Describe the morphology of the erythrocytes.
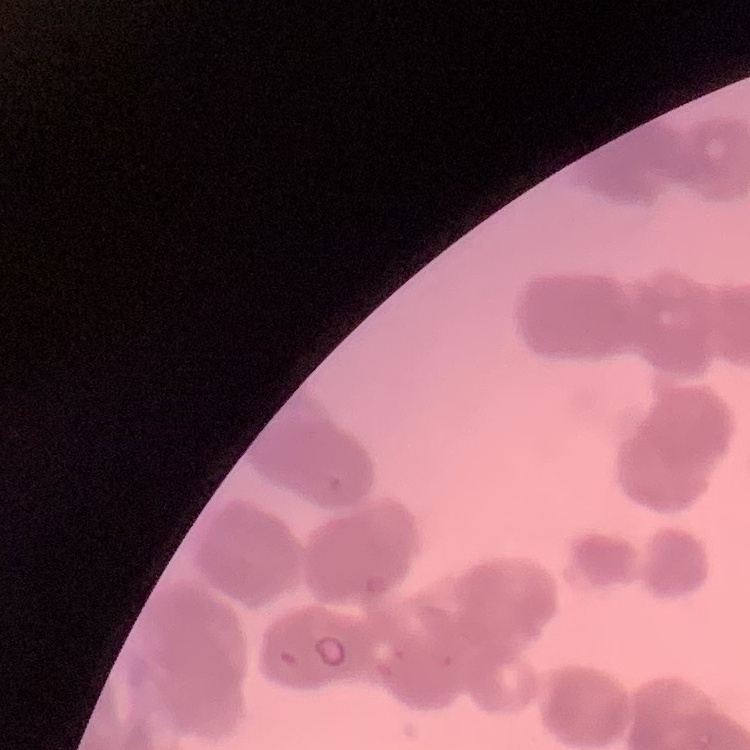

Rouleaux formation.

One tile cut from a larger photomicrograph. Field's or Giemsa stain. Thin peripheral smear.